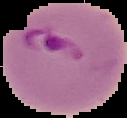

preparation = thin blood film
image size = 127×118 pixels
result = Plasmodium parasites detected
image type = segmented cell region on a black background